Outline each blood parasite and name the species.
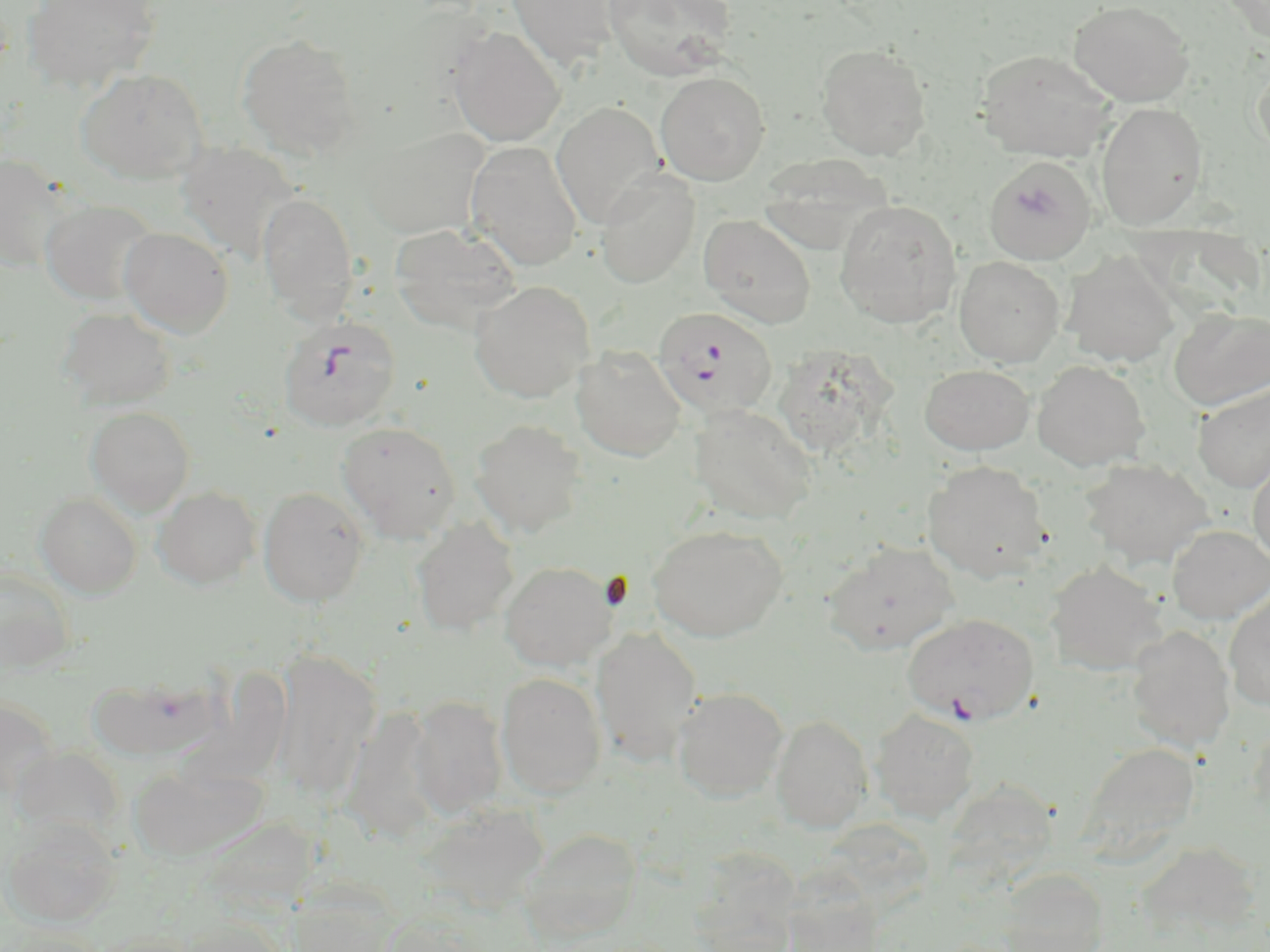

Approximate bounding boxes as (x1,y1)-(x2,y2) corner pairs in pixels.
Plasmodium falciparum-infected red blood cells: (652,306)-(778,420), (277,315)-(402,432).
No Plasmodium ovale, Plasmodium malariae, Plasmodium vivax, Babesia divergens, or Trypanosoma brucei observed.

slide-level diagnosis = Plasmodium falciparum
preparation = thin blood film
modality = light microscopy
image size = 1270×952 pixels
uninfected red blood cell locations = approximate bounding boxes as (x1,y1)-(x2,y2) corner pairs in pixels: (22,0)-(162,92), (507,0)-(620,70), (603,0)-(736,81), (1068,0)-(1194,106), (1222,0)-(1270,43), (449,26)-(566,147), (237,33)-(362,159), (816,43)-(932,160), (975,49)-(1118,162), (1250,56)-(1270,160), (76,68)-(207,183), (655,71)-(771,185), (551,101)-(665,229), (1096,102)-(1208,229), (359,127)-(490,239), (465,141)-(582,270), (177,142)-(303,264), (757,153)-(894,255), (0,155)-(75,273), (983,156)-(1097,265), (596,168)-(701,288), (257,192)-(359,324), (40,199)-(159,306), (835,199)-(962,328), (698,213)-(817,328), (388,222)-(522,334), (118,227)-(233,337), (1063,249)-(1180,368), (954,256)-(1065,367), (469,281)-(595,403), (58,307)-(177,410), (1168,307)-(1270,411), (789,341)-(891,461), (571,346)-(687,461), (1032,360)-(1150,471), (920,364)-(1034,455), (1192,384)-(1270,492), (688,403)-(817,525), (85,406)-(195,515), (470,419)-(587,538), (337,421)-(461,542), (1248,453)-(1270,567), (1079,457)-(1213,569), (922,460)-(1052,582), (153,485)-(261,589), (258,486)-(370,606), (35,491)-(142,597), (411,517)-(519,637), (648,524)-(787,642), (1167,525)-(1270,625), (822,542)-(961,656), (500,560)-(618,671), (1045,560)-(1167,677), (0,566)-(77,674), (1223,587)-(1270,712), (902,612)-(1040,726), (1127,625)-(1235,752), (591,627)-(702,764), (272,652)-(381,801), (185,666)-(298,794), (497,672)-(607,798), (88,676)-(224,761), (673,686)-(789,801), (408,695)-(509,818), (0,698)-(59,800), (346,699)-(441,846), (870,708)-(979,822), (770,714)-(873,833), (1248,721)-(1270,823), (1077,741)-(1200,861), (130,762)-(268,862), (416,802)-(550,916), (3,819)-(121,927), (519,827)-(642,943), (1135,841)-(1261,939), (688,848)-(802,952), (998,868)-(1109,952), (781,871)-(886,951), (281,886)-(401,950), (176,917)-(286,952), (86,929)-(201,952)
magnification = 1000x
stain = May-Grünwald-Giemsa
field of view = single